State which parasite is depicted.
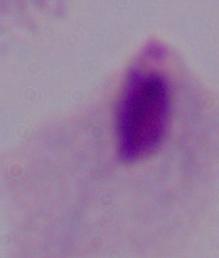
A trichomonad.

Summary:
  - Modality: micrograph
  - Magnification: 1000x